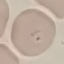 Result: malaria parasites detected. Acquired by smartphone through the microscope eyepiece. Automatically extracted cell patch, resized to 64 × 64 pixels. Thin blood smear. Giemsa stain.